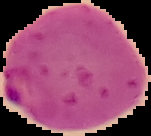 Cell region segmented out of the field of view; the surrounding area is masked to black. Image is 151×136 pixels. Result: Plasmodium parasites detected. From a thin blood film.